Comment on the morphology of the red blood cells.
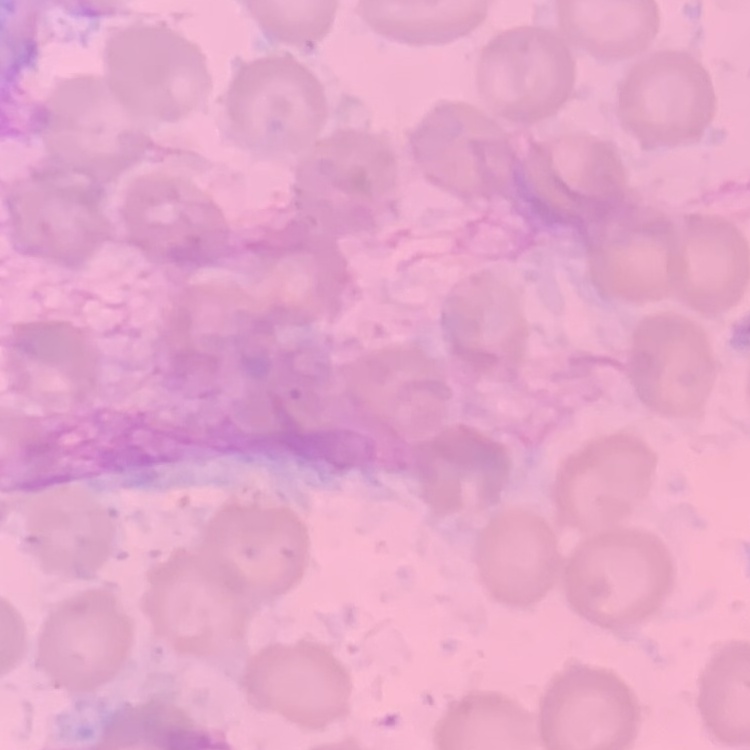
No rouleaux formation.

preparation = thin peripheral smear
image type = square crop of a larger photomicrograph
stain = Field's or Giemsa